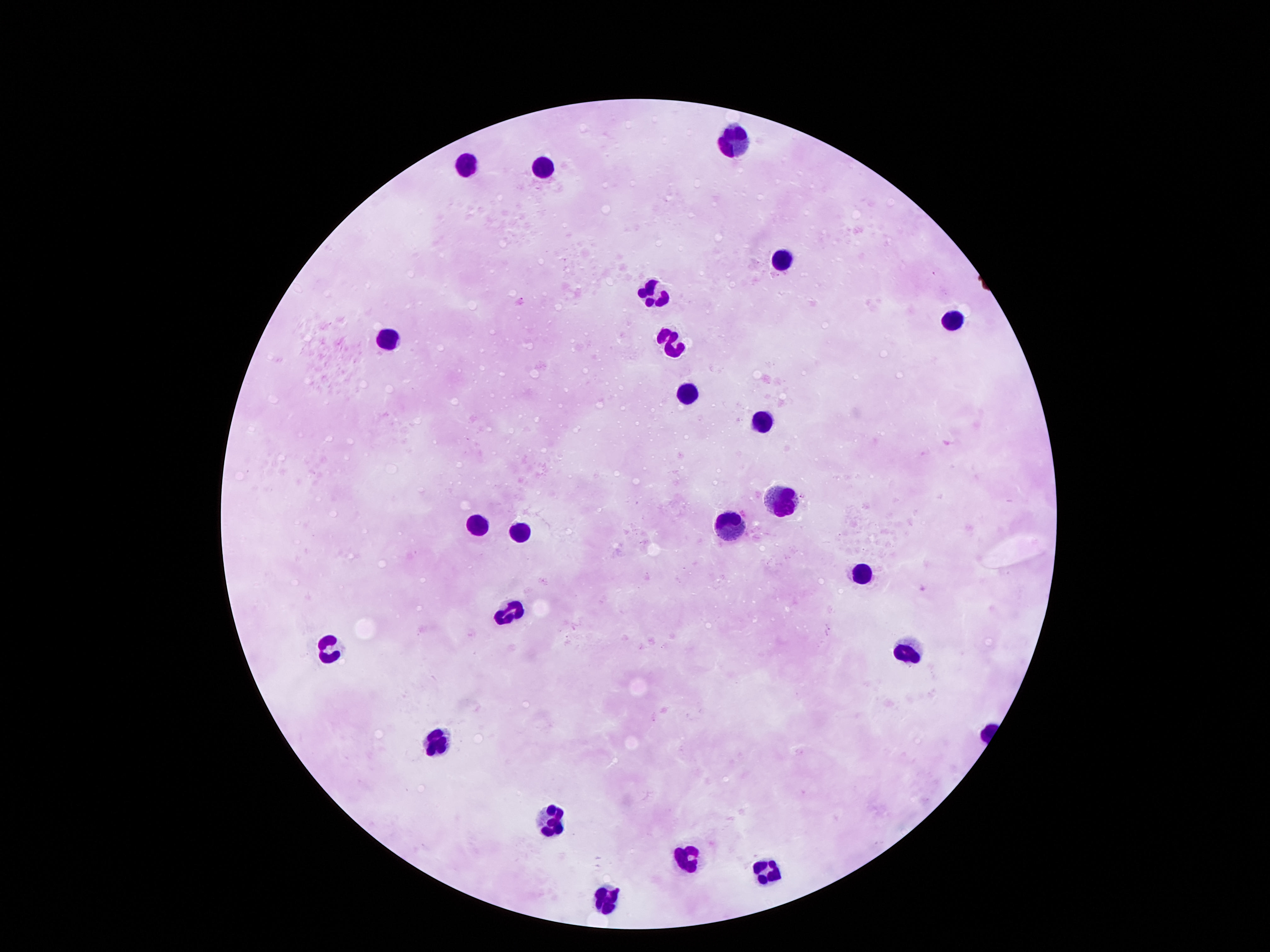
Approximate object centers, in pixels from the top-left corner.
Summary:
  - Leukocyte locations: (x=735, y=139), (x=470, y=163), (x=539, y=170), (x=776, y=257), (x=652, y=295), (x=956, y=319), (x=387, y=336), (x=669, y=338), (x=687, y=394), (x=761, y=419), (x=780, y=499), (x=477, y=526), (x=732, y=529), (x=517, y=535), (x=862, y=572), (x=508, y=613), (x=326, y=644), (x=903, y=647), (x=435, y=749), (x=548, y=825), (x=681, y=857), (x=768, y=873), (x=598, y=899)
  - Field of view: single
  - Capture: smartphone camera through the microscope eyepiece
  - Image size: 1270×952 pixels
  - Preparation: thick blood smear
  - Magnification: 100x
  - Patient malaria status: negative
  - Stain: Giemsa